Report the malaria status of this cell.
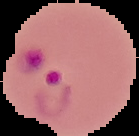
It is parasitized.

From a thin blood smear. Image is 139×136 pixels. Cell region segmented out of the field of view; the surrounding area is masked to black.